Name the parasite shown.
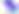
This is Toxoplasma gondii.

modality: photomicrograph
magnification: 400x